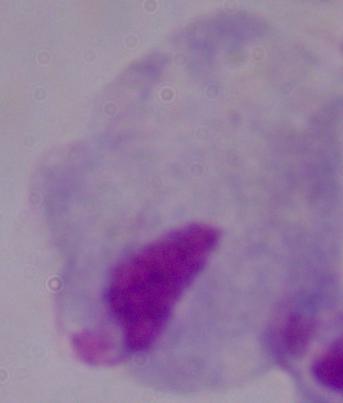 1000x magnification. A trichomonad is seen. Photomicrograph.